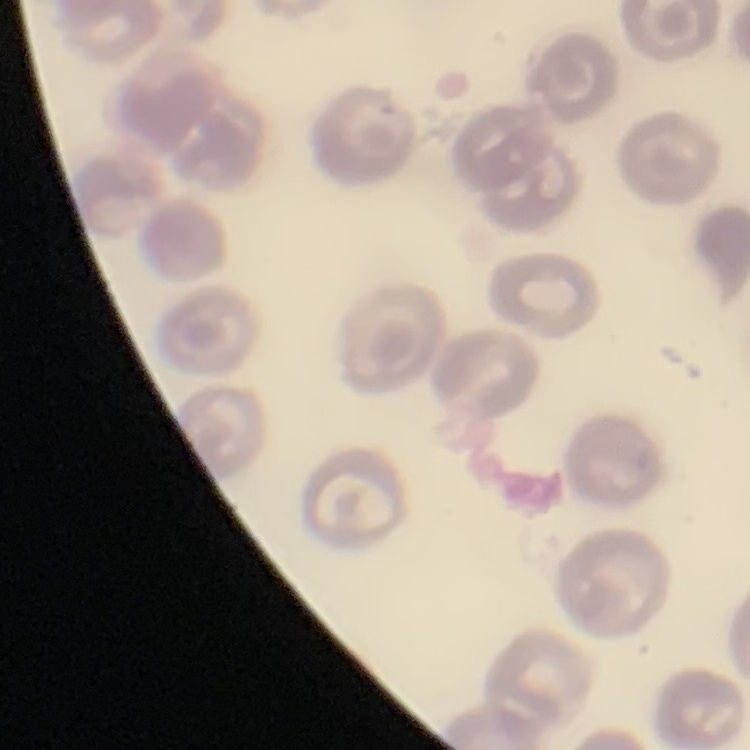

Summary:
  - Red blood cell morphology: no rouleaux formation
  - Preparation: thin blood smear
  - Stain: Field's or Giemsa
  - Image type: one tile cut from a larger photomicrograph